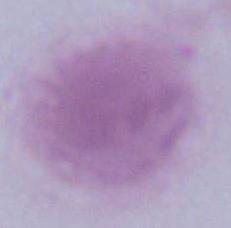
Captured at 1000x magnification. Micrograph. A red blood cell is shown.